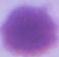

modality = micrograph
magnification = 1000x
identification = red blood cell